Report the malaria status of this cell.
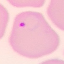

Parasitized.

{
  "preparation": "thin blood film",
  "stain": "Giemsa",
  "capture": "smartphone through the microscope eyepiece",
  "image_type": "automatically extracted cell patch, resized to 64 × 64 pixels"
}